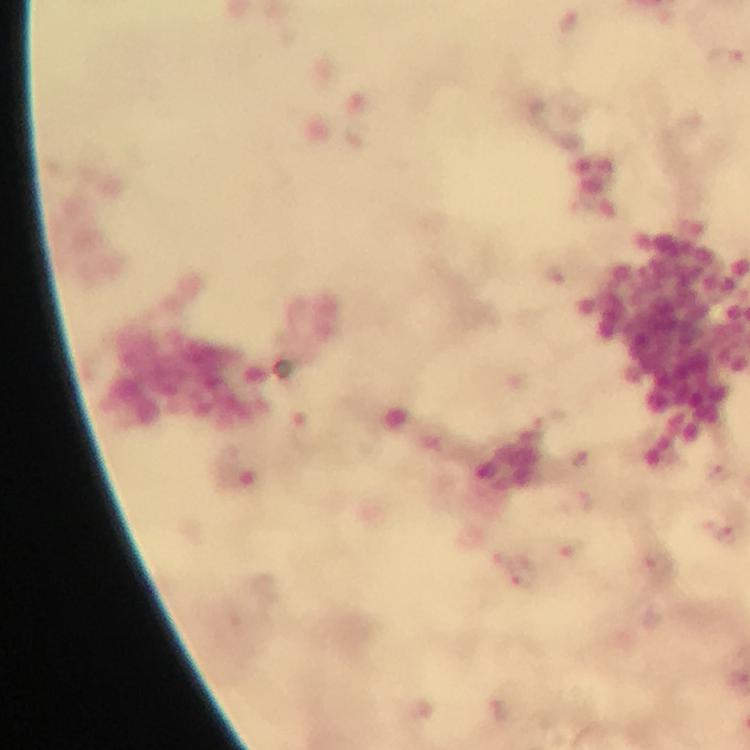 Approximate centers as {x, y} in pixels. Plasmodium parasite locations: {725, 57}, {555, 274}, {583, 460}, {718, 474}, {583, 500}, {726, 534}, {572, 547}, {523, 576}, {497, 710}. Giemsa stain. Image is 750×750 pixels. Photographed with a smartphone mounted on the microscope. Thick blood film. At 100x magnification. Immersion oil was used. From a malaria diagnostic workup. Cropped region of a single field of view.